Assess this cell for malaria.
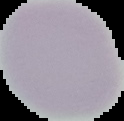
It is uninfected.

From a thin blood smear. The area outside the segmented cell region is set to black. Image is 124×121 pixels.